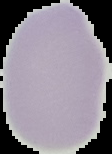

Summary:
  - Preparation: thin blood smear
  - Image type: segmented cell region on a black background
  - Image size: 112×154 pixels
  - Malaria status: uninfected